Identify the parasite.
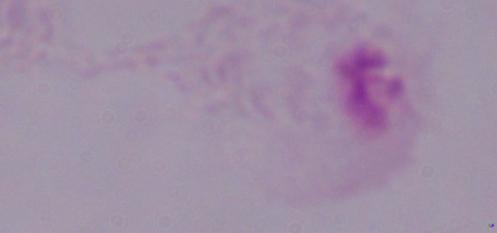
This is a trichomonad.

Micrograph. 1000x magnification.